Name the cell type shown.
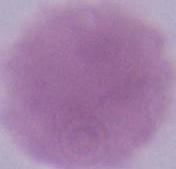

This is an erythrocyte.

Summary:
  - Magnification: 1000x
  - Modality: photomicrograph